Assess this cell for malaria.
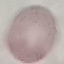

It is uninfected.

Summary:
  - Stain: Giemsa
  - Preparation: thin blood smear
  - Image type: cell patch, automatically extracted from a larger field of view and resized to 64 × 64 pixels
  - Capture: smartphone through the microscope eyepiece